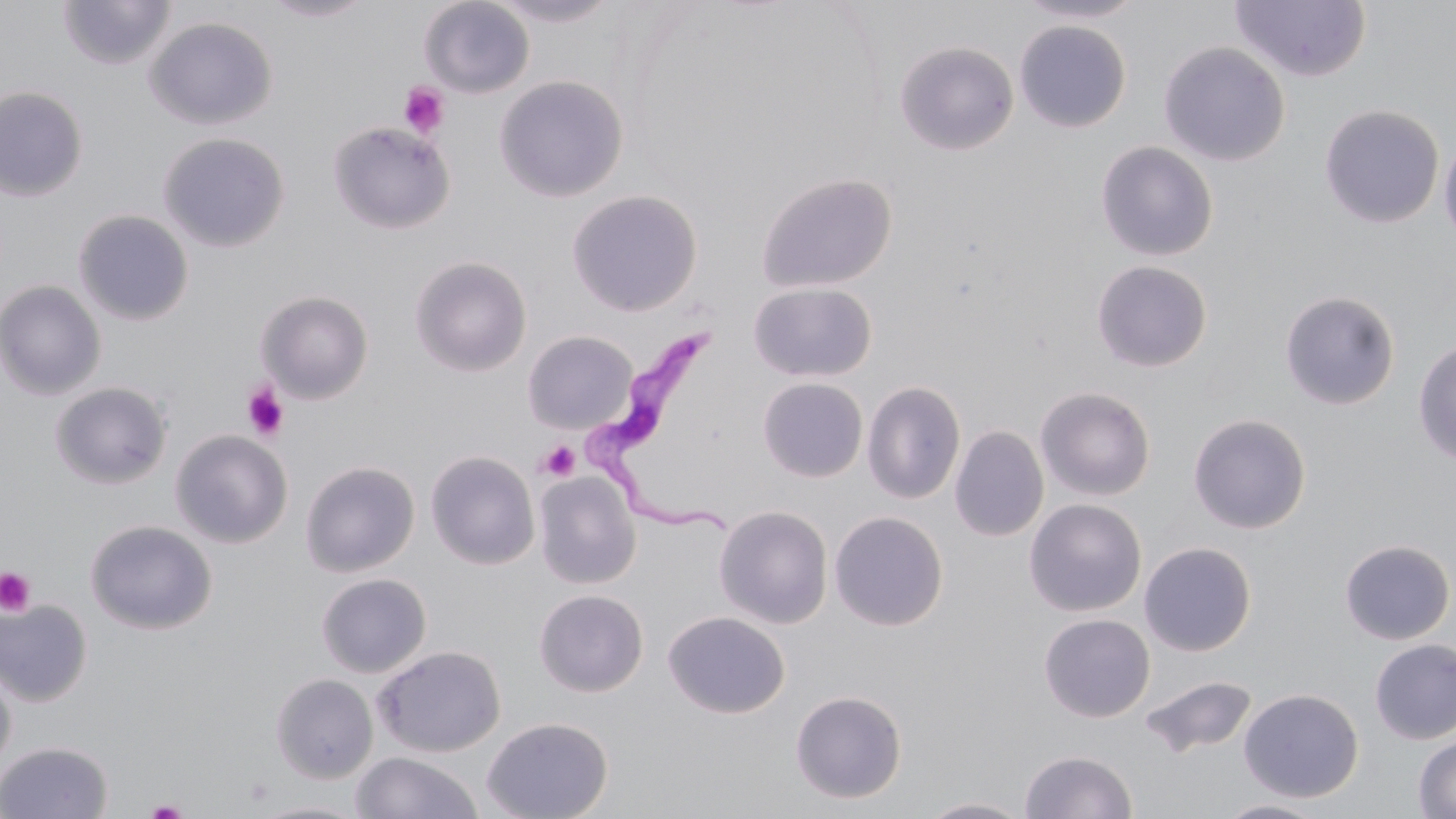

slide-level diagnosis = Trypanosoma brucei
platelet locations = approximate bounding boxes as (x1,y1)-(x2,y2) corner pairs in pixels: (397,81)-(450,139), (242,382)-(289,442), (538,441)-(580,481), (0,567)-(36,617), (143,798)-(191,818)
field of view = single
stain = May-Grünwald-Giemsa
magnification = 1000x
Trypanosoma brucei locations = approximate bounding boxes as (x1,y1)-(x2,y2) corner pairs in pixels: (576,320)-(739,540)
image size = 1456×819 pixels
preparation = thin blood smear
uninfected red blood cell locations = approximate bounding boxes as (x1,y1)-(x2,y2) corner pairs in pixels: (57,0)-(177,70), (258,0)-(378,22), (419,0)-(535,98), (488,0)-(623,27), (1013,0)-(1147,24), (1231,1)-(1372,83), (144,17)-(278,130), (1014,20)-(1131,133), (895,41)-(1019,155), (1158,41)-(1290,165), (494,76)-(628,202), (0,86)-(87,201), (1319,104)-(1444,228), (328,121)-(455,234), (1439,131)-(1456,250), (158,133)-(289,252), (1096,141)-(1218,261), (756,172)-(897,292), (567,190)-(703,317), (73,209)-(194,326), (410,255)-(531,376), (1091,260)-(1213,372), (0,280)-(106,401), (748,281)-(877,382), (1279,290)-(1400,410), (256,291)-(374,404), (522,330)-(638,435), (1413,338)-(1456,467), (757,377)-(868,483), (862,380)-(966,504), (49,381)-(172,490), (1035,386)-(1156,501), (1188,413)-(1311,534), (950,425)-(1049,542), (171,429)-(293,548), (425,450)-(540,569), (300,460)-(419,577), (534,472)-(641,589), (1024,499)-(1147,617), (714,505)-(833,629), (829,511)-(948,630), (85,520)-(217,635), (1339,539)-(1455,645), (1139,541)-(1256,656), (316,573)-(431,678), (534,589)-(648,696), (0,599)-(93,707), (664,611)-(789,718), (1039,613)-(1155,723), (1370,638)-(1456,745), (373,644)-(506,757), (0,659)-(16,775), (271,673)-(378,783), (1139,675)-(1258,760), (1238,688)-(1364,803), (790,690)-(907,803), (481,716)-(613,819), (1413,733)-(1456,818), (0,741)-(113,819), (1020,749)-(1137,818), (352,751)-(483,818), (917,797)-(1034,818), (246,799)-(372,819), (1216,799)-(1329,818)
modality = optical microscopy